Give the position of every leukocyte visible.
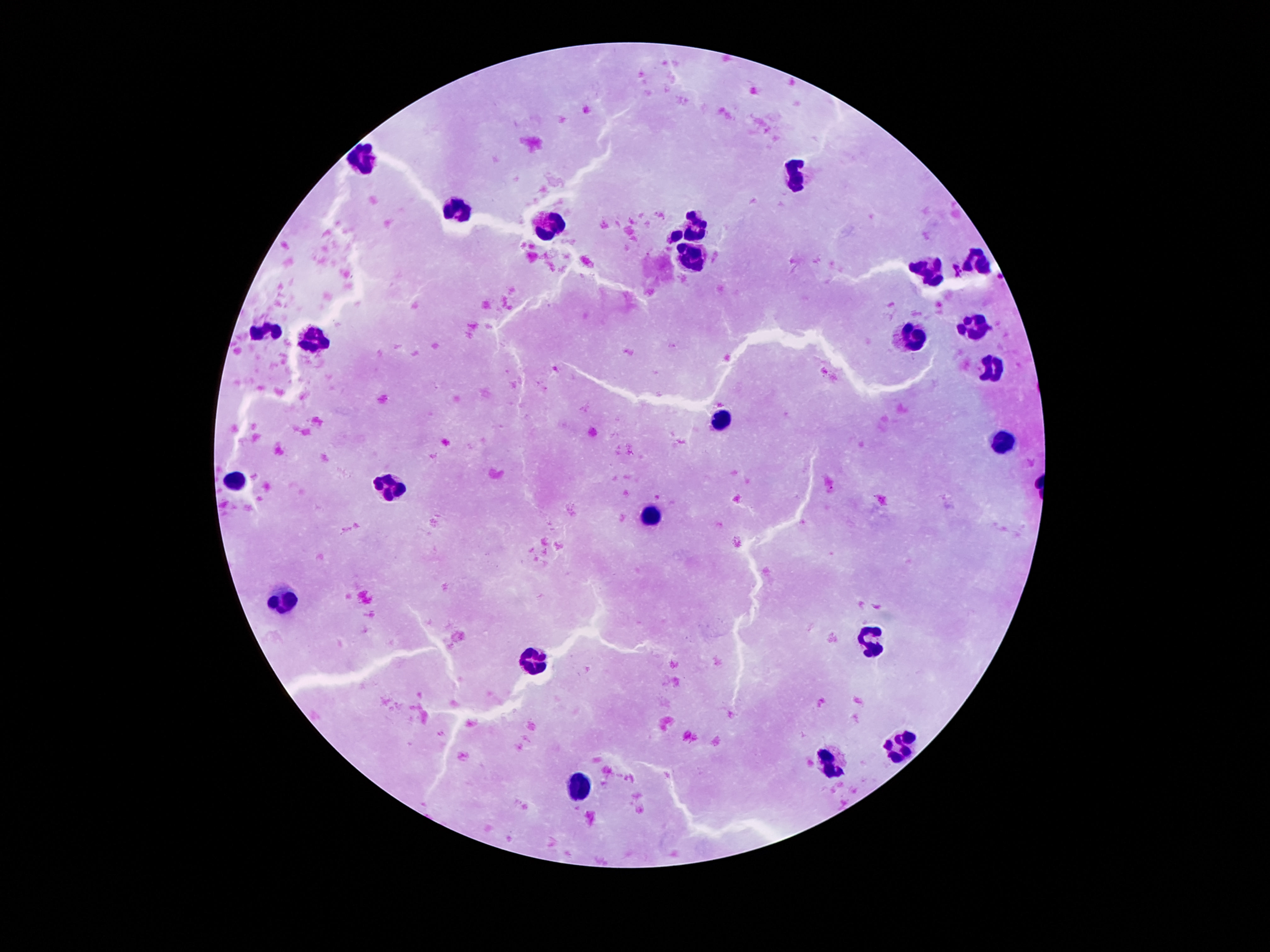

Approximate centers as [x, y] in pixels.
Leukocytes: [365, 159], [799, 171], [459, 212], [552, 222], [688, 226], [692, 259], [975, 262], [930, 271], [975, 327], [267, 329], [317, 337], [912, 338], [995, 370], [718, 418], [1002, 444], [235, 483], [387, 486], [652, 515], [279, 593], [870, 642], [536, 665], [902, 746], [832, 763], [576, 785].

Summary:
  - Preparation: thick peripheral-blood smear
  - Image size: 1270×952 pixels
  - Magnification: 100x
  - Field of view: one from this slide
  - Capture: smartphone camera through the microscope eyepiece
  - Patient malaria status: not infected
  - Stain: Giemsa